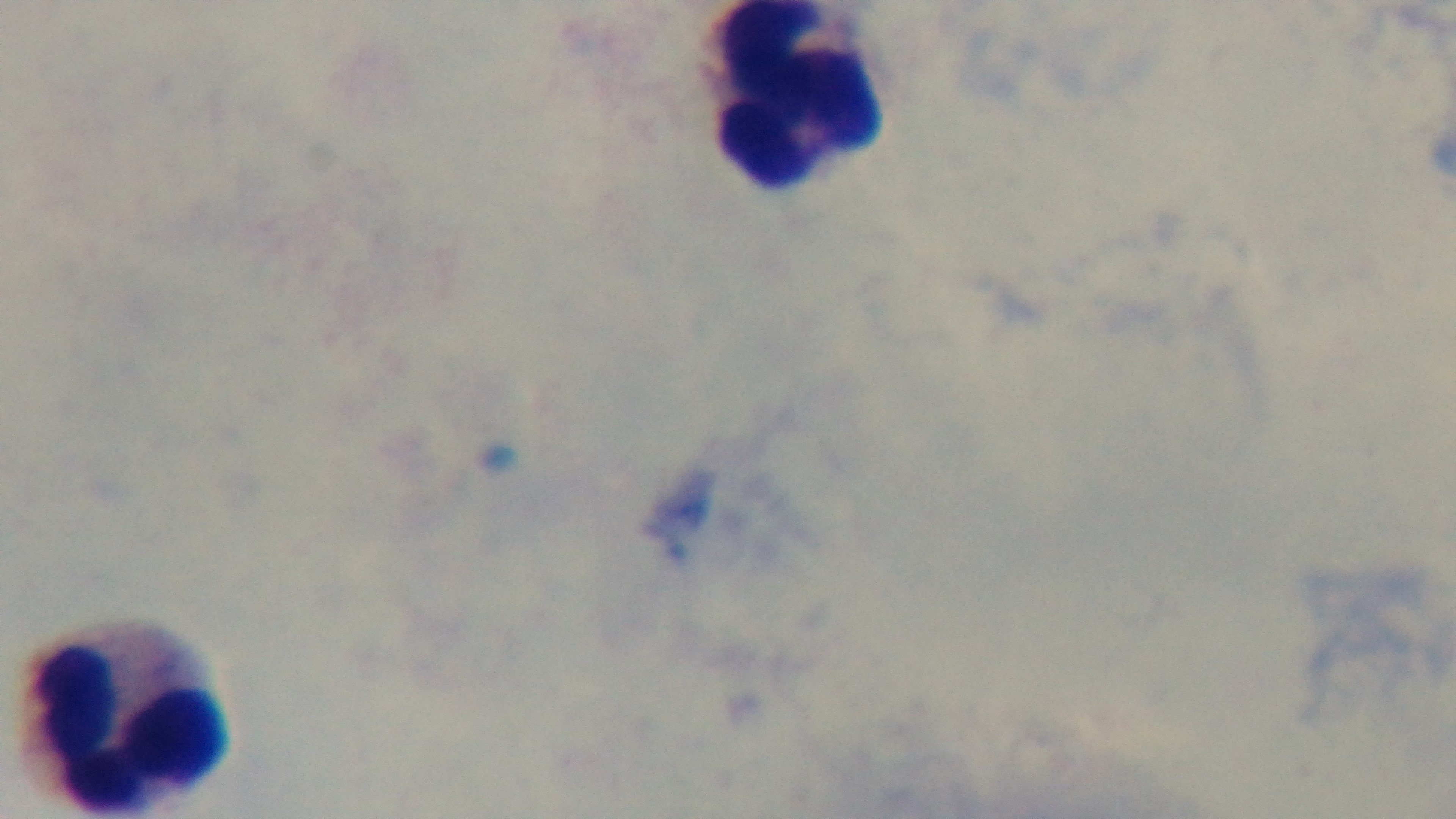
Summary:
  - Objective: 100x oil immersion
  - Preparation: thick
  - Capture: mounted 4K digital camera
  - Modality: light microscopy
  - Malaria status: negative
  - Field of view: one from the slide
  - Stain: Giemsa